Point out each malaria parasite.
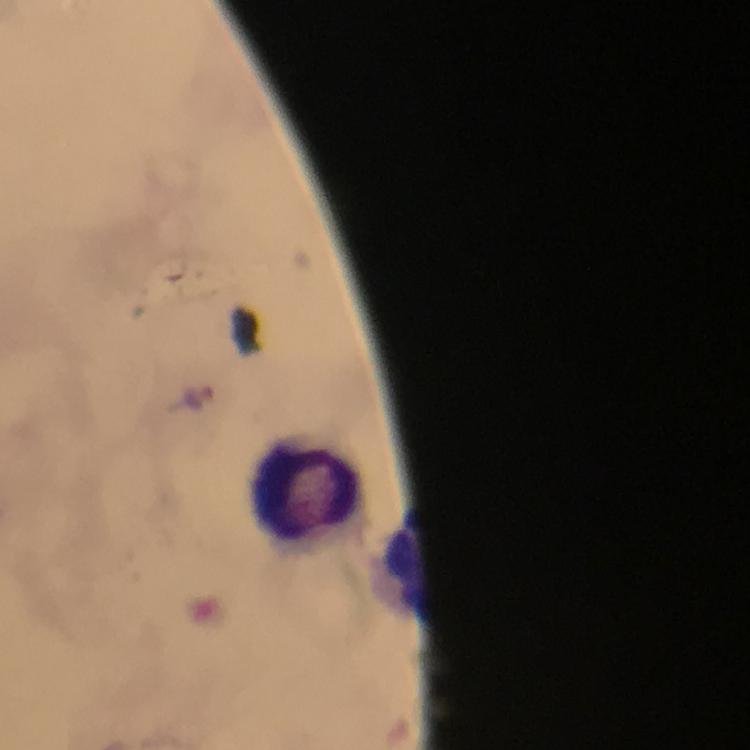

No malaria parasites seen.

Approximate centers as [x, y] in pixels. Leukocyte locations: [308, 488]. Immersion oil applied. Image is 750×750 pixels. From a diagnostic examination for malaria. At 100x magnification. Cropped region of a single field of view. Giemsa-stained preparation. Photographed with a smartphone mounted on the microscope. Thick blood smear.